Point out each Plasmodium parasite.
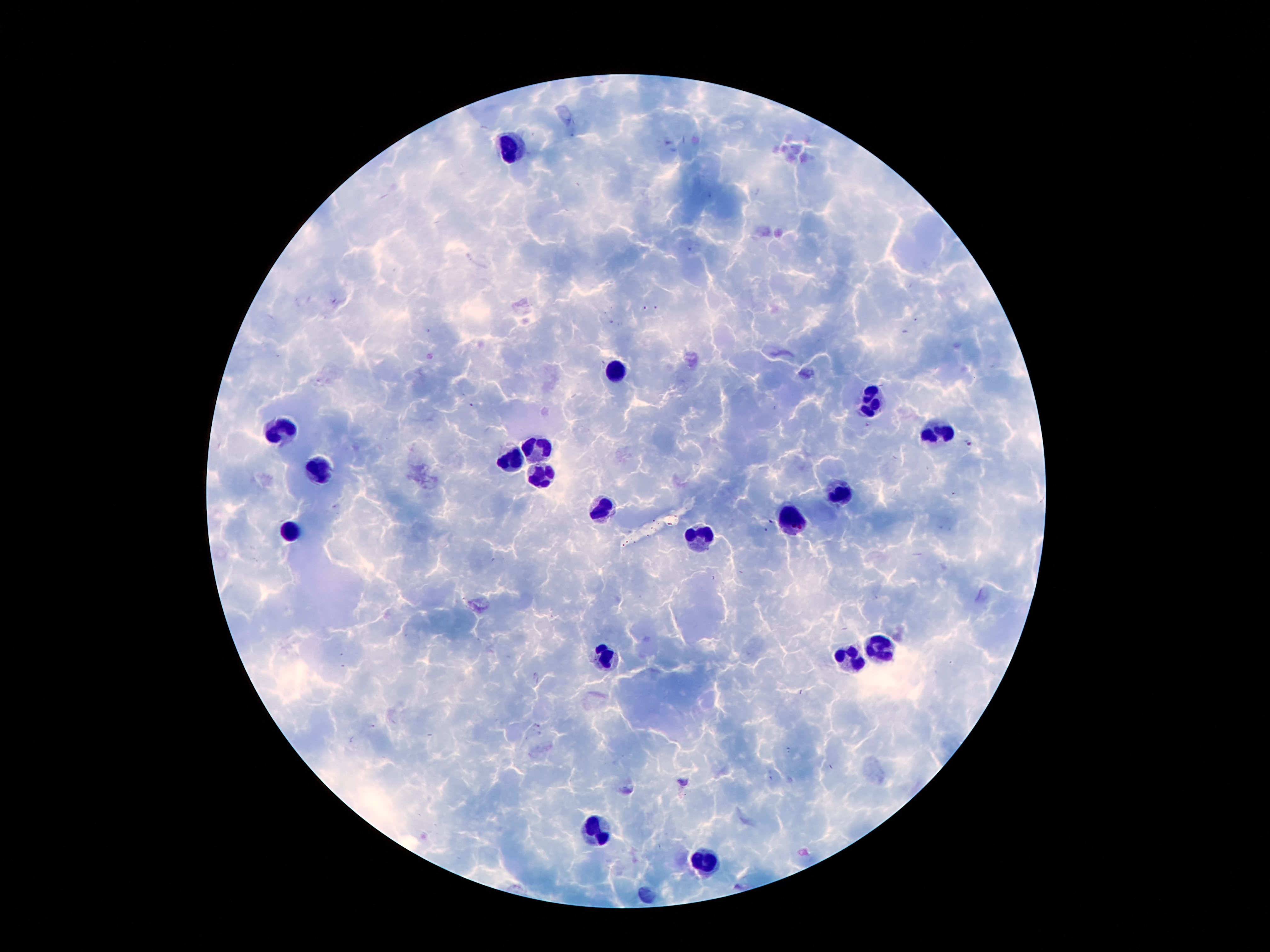
Approximate centers as (x, y) in pixels.
Plasmodium parasites: (969, 443), (771, 521), (766, 531).

Summary:
  - Leukocyte locations: (513, 148), (612, 371), (871, 402), (283, 433), (938, 435), (535, 445), (510, 461), (324, 466), (543, 476), (836, 496), (602, 509), (795, 522), (291, 532), (701, 534), (882, 644), (604, 656), (851, 659), (597, 832), (709, 863)
  - Magnification: 100x
  - Field of view: single
  - Patient malaria status: infected with Plasmodium falciparum
  - Capture: smartphone through the microscope eyepiece
  - Image size: 1270×952 pixels
  - Stain: Giemsa
  - Preparation: thick peripheral-blood smear